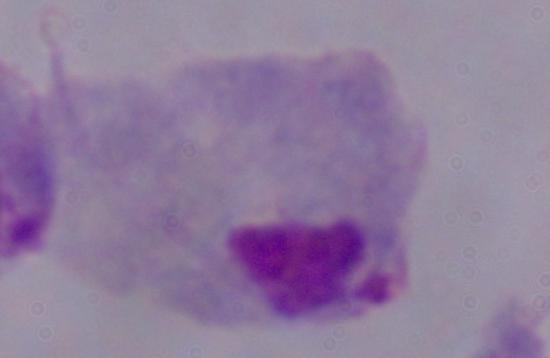 Micrograph. 1000x magnification. A trichomonad is seen.